Outline each Plasmodium falciparum-infected red blood cell.
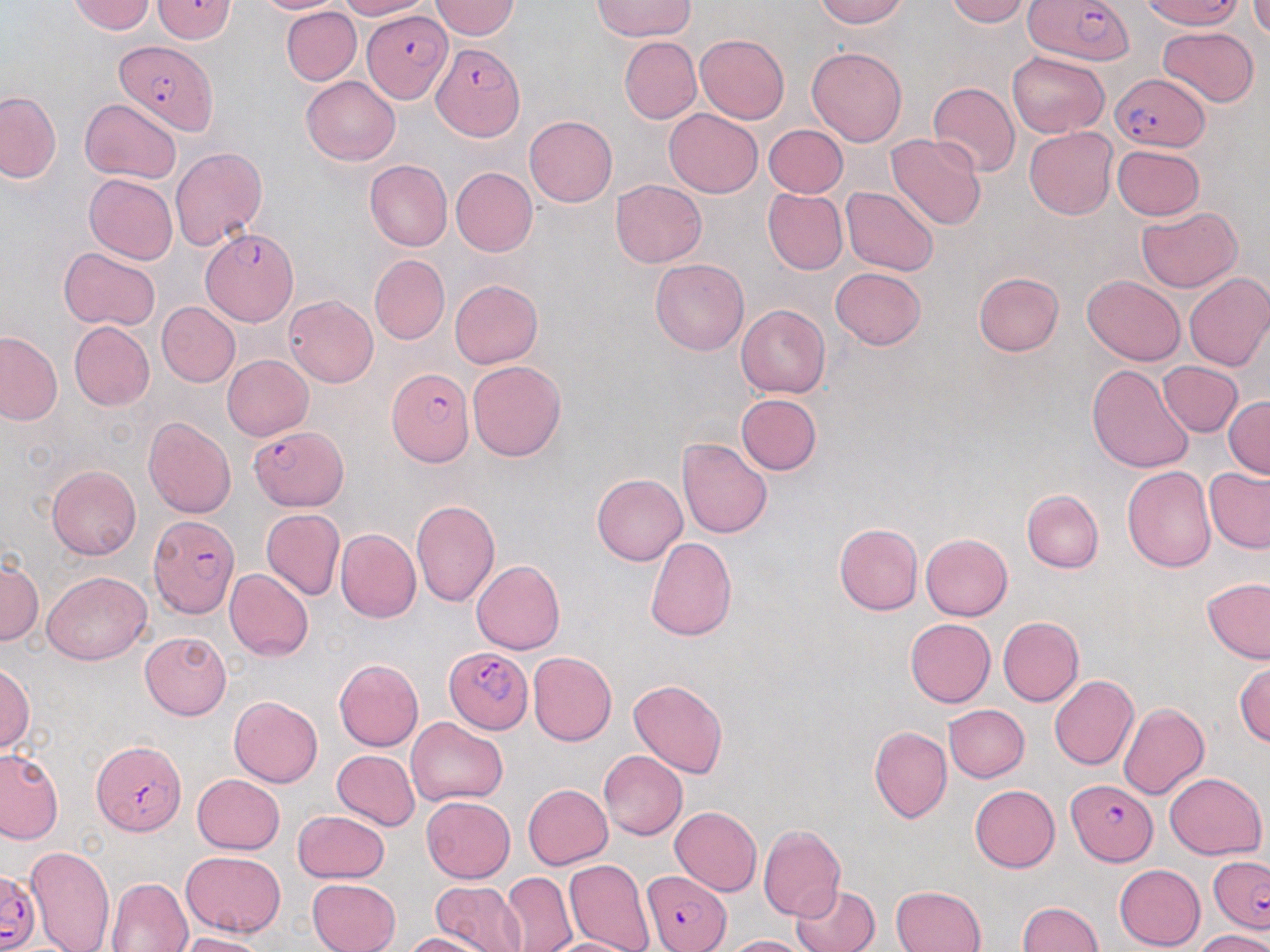

Approximate bounding boxes as (x1,y1)-(x2,y2) corner pairs in pixels.
Plasmodium falciparum-infected red blood cells: (152,0)-(236,43), (1021,0)-(1138,65), (1140,0)-(1246,30), (363,10)-(453,101), (115,39)-(216,135), (433,42)-(525,142), (1109,73)-(1210,151), (199,227)-(297,326), (387,369)-(474,467), (249,425)-(349,511), (148,515)-(240,618), (444,646)-(535,733), (91,740)-(186,836), (1068,780)-(1158,866), (1210,856)-(1270,932), (0,870)-(38,951), (642,870)-(731,951).

slide-level diagnosis = Plasmodium falciparum
image size = 1270×952 pixels
preparation = thin blood film
uninfected red blood cell locations = approximate bounding boxes as (x1,y1)-(x2,y2) corner pairs in pixels: (251,0)-(345,14), (337,0)-(430,20), (591,0)-(697,43), (815,0)-(907,27), (944,0)-(1029,26), (1249,0)-(1270,40), (67,1)-(156,34), (431,1)-(519,39), (282,6)-(361,85), (1157,26)-(1260,107), (695,34)-(789,123), (619,36)-(701,123), (807,47)-(907,146), (1006,51)-(1109,137), (301,77)-(399,166), (928,82)-(1020,176), (0,91)-(61,183), (80,98)-(181,183), (663,109)-(763,198), (524,115)-(617,208), (763,124)-(848,197), (1024,126)-(1117,219), (886,134)-(988,231), (1111,145)-(1206,220), (170,146)-(267,252), (366,160)-(452,252), (451,166)-(537,256), (84,174)-(177,263), (611,179)-(707,267), (841,187)-(938,276), (762,190)-(847,274), (1135,207)-(1243,293), (59,246)-(161,330), (369,254)-(449,344), (651,258)-(748,355), (829,268)-(927,350), (1182,271)-(1270,371), (973,272)-(1064,355), (1083,275)-(1185,365), (449,279)-(543,368), (285,294)-(379,387), (156,302)-(240,387), (736,304)-(830,399), (69,321)-(154,410), (0,332)-(62,424), (222,355)-(313,440), (467,360)-(567,461), (1157,361)-(1244,437), (1086,364)-(1194,473), (735,394)-(822,476), (1225,396)-(1269,480), (143,416)-(236,518), (678,438)-(773,538), (47,464)-(141,560), (1123,466)-(1217,572), (1205,467)-(1270,553), (592,473)-(687,565), (1022,490)-(1103,572), (411,500)-(500,605), (261,508)-(344,600), (833,522)-(922,614), (335,528)-(421,623), (921,533)-(1012,621), (645,536)-(737,642), (0,557)-(43,646), (470,560)-(565,655), (224,569)-(315,661), (43,570)-(150,664), (1202,578)-(1270,664), (997,617)-(1084,706), (905,618)-(995,707), (139,631)-(232,720), (528,651)-(616,745), (333,658)-(424,751), (1234,661)-(1270,747), (0,663)-(35,753), (1049,675)-(1139,770), (629,679)-(727,777), (229,696)-(322,787), (1118,701)-(1209,799), (944,704)-(1030,782), (406,718)-(508,806), (869,726)-(951,824), (0,748)-(64,844), (332,750)-(421,831), (599,750)-(687,840), (1163,772)-(1266,859), (191,773)-(286,854), (522,784)-(613,869), (970,784)-(1060,873), (421,795)-(516,883), (670,806)-(762,895), (292,810)-(391,883), (757,825)-(845,921), (24,846)-(116,952), (182,850)-(285,937), (563,858)-(655,952), (1114,864)-(1205,950), (500,871)-(577,952), (106,877)-(194,952), (308,878)-(400,952), (429,880)-(527,952), (791,883)-(880,952), (892,884)-(986,952), (1016,902)-(1102,952), (1195,930)-(1270,952), (403,931)-(494,952), (171,932)-(268,952), (720,935)-(812,952), (537,936)-(647,952)
magnification = 1000x
field of view = single
stain = May-Grünwald-Giemsa
modality = light microscopy